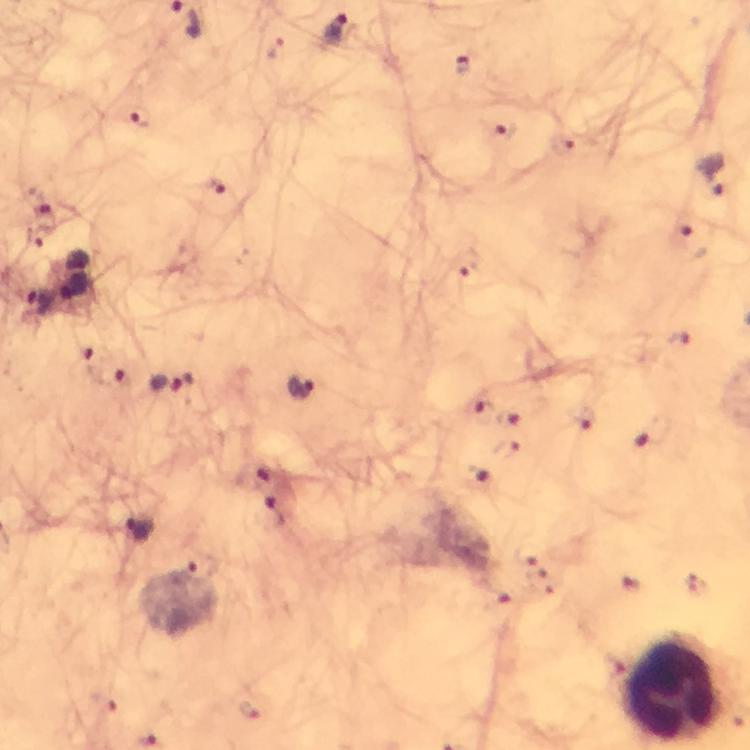
leukocyte locations = approximate centers as [x, y] in pixels: [675, 692]
image size = 750×750 pixels
context = from a malaria diagnostic workup
magnification = 100x
capture = smartphone mounted on the microscope
Plasmodium parasite locations = approximate centers as [x, y] in pixels: [337, 32], [463, 67], [139, 116], [501, 131], [565, 143], [715, 175], [216, 185], [44, 215], [692, 242], [468, 271], [677, 341], [81, 348], [111, 376], [172, 385], [304, 389], [481, 412], [517, 419], [583, 419], [656, 437], [506, 453], [255, 472], [480, 479], [275, 509], [138, 530], [104, 700], [249, 709]
cropped from = a single field of view
preparation = thick blood smear
immersion oil = applied
stain = Giemsa